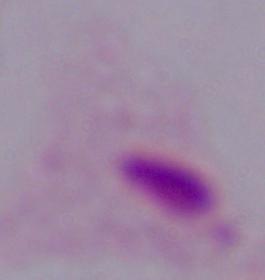

Summary:
  - Magnification: 1000x
  - Modality: micrograph
  - Identification: trichomonad